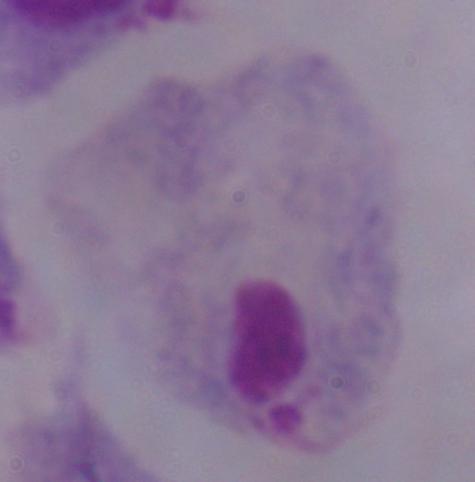

Captured at 1000x magnification. A trichomonad is shown. Micrograph.